Outline each blood parasite and name the species.
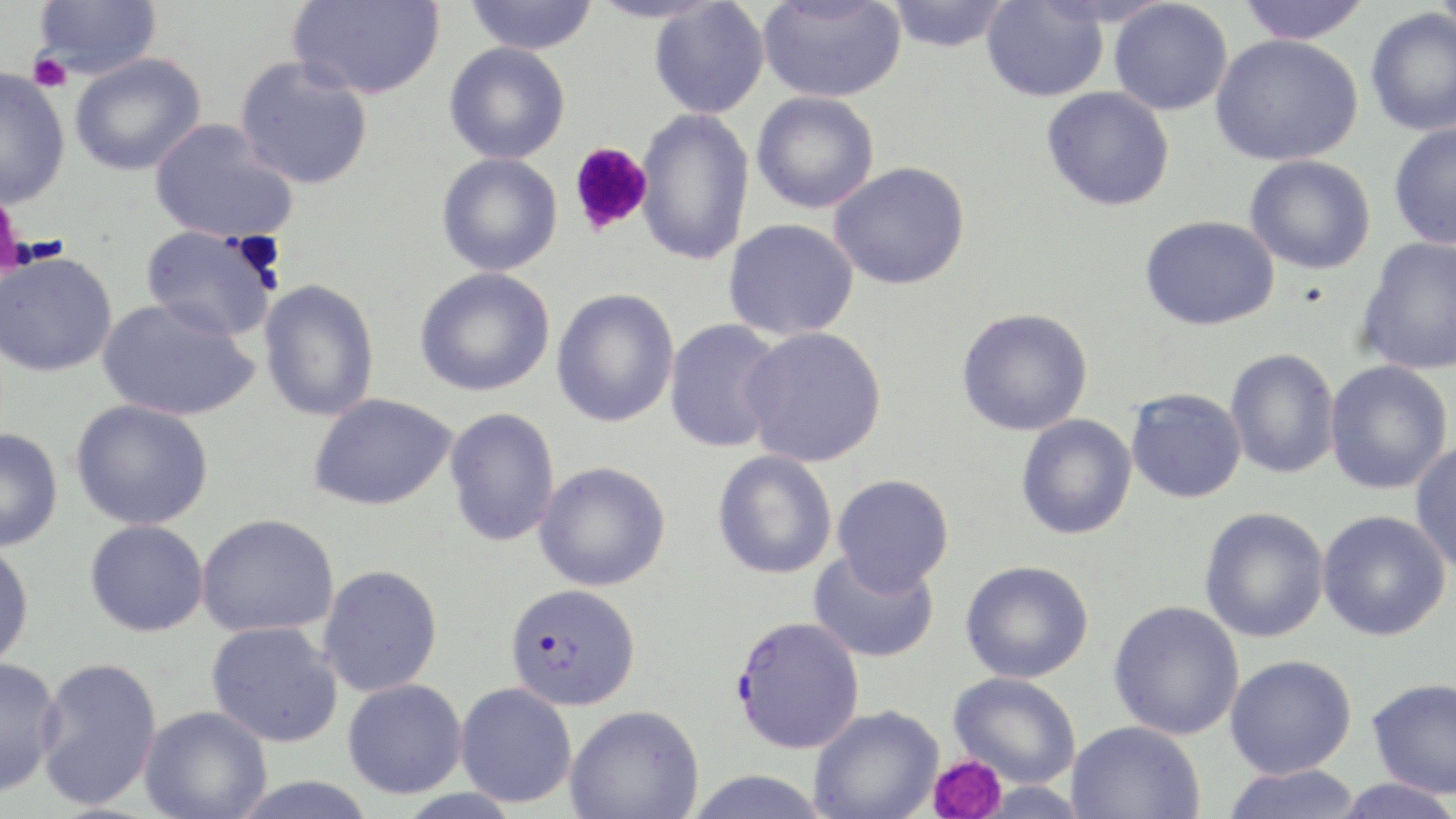
Approximate bounding boxes as (x1, y1, x2, y2) in pixels.
Plasmodium falciparum-infected red blood cells: (505, 583, 641, 711), (730, 615, 865, 753).
No Plasmodium ovale, Plasmodium malariae, Plasmodium vivax, Babesia divergens, or Trypanosoma brucei observed.

Summary:
  - Uninfected red blood cell locations: (33, 0, 163, 80), (287, 0, 445, 100), (465, 0, 599, 55), (586, 0, 724, 24), (649, 0, 770, 118), (758, 0, 906, 103), (886, 0, 1012, 52), (1237, 0, 1372, 44), (1434, 0, 1456, 43), (982, 1, 1108, 102), (1109, 1, 1233, 116), (1365, 7, 1456, 136), (1210, 33, 1363, 166), (444, 42, 570, 164), (70, 54, 207, 176), (234, 56, 373, 190), (0, 67, 70, 209), (1041, 86, 1175, 211), (751, 91, 880, 214), (635, 108, 754, 266), (149, 119, 297, 244), (1388, 123, 1456, 249), (436, 153, 562, 276), (1244, 155, 1376, 274), (829, 161, 970, 290), (1140, 215, 1279, 330), (723, 218, 860, 341), (140, 224, 281, 342), (1356, 237, 1456, 376), (0, 251, 118, 377), (414, 267, 555, 397), (259, 279, 380, 422), (551, 289, 679, 427), (97, 297, 259, 422), (956, 307, 1093, 436), (664, 318, 786, 453), (740, 326, 887, 467), (1225, 348, 1340, 479), (1325, 360, 1453, 495), (1126, 388, 1247, 503), (308, 393, 458, 510), (70, 399, 214, 530), (444, 407, 560, 547), (1016, 414, 1137, 540), (0, 427, 63, 552), (1410, 441, 1456, 575), (712, 450, 838, 579), (535, 461, 671, 591), (832, 474, 954, 593), (1199, 507, 1329, 643), (1317, 510, 1451, 641), (196, 513, 339, 638), (84, 519, 208, 637), (0, 540, 34, 671), (808, 549, 940, 663), (960, 560, 1093, 684), (318, 564, 443, 697), (1108, 600, 1245, 740), (206, 621, 343, 748), (1225, 654, 1357, 778), (0, 656, 64, 797), (34, 656, 162, 809), (949, 672, 1081, 788), (343, 678, 467, 799), (1367, 678, 1456, 799), (455, 682, 578, 808), (564, 705, 704, 819), (809, 705, 943, 819), (139, 706, 272, 819), (1066, 720, 1204, 818), (1222, 764, 1364, 819), (685, 769, 831, 818), (228, 775, 378, 819), (1331, 778, 1456, 818)
  - Platelet locations: (27, 51, 71, 92), (568, 143, 653, 237), (0, 204, 30, 274), (233, 231, 286, 280), (928, 754, 1007, 818)
  - Slide-level diagnosis: Plasmodium falciparum
  - Field of view: single
  - Image size: 1456×819 pixels
  - Stain: May-Grünwald-Giemsa
  - Magnification: 1000x
  - Modality: light microscopy
  - Preparation: thin blood smear